Describe the morphology of the red blood cells.
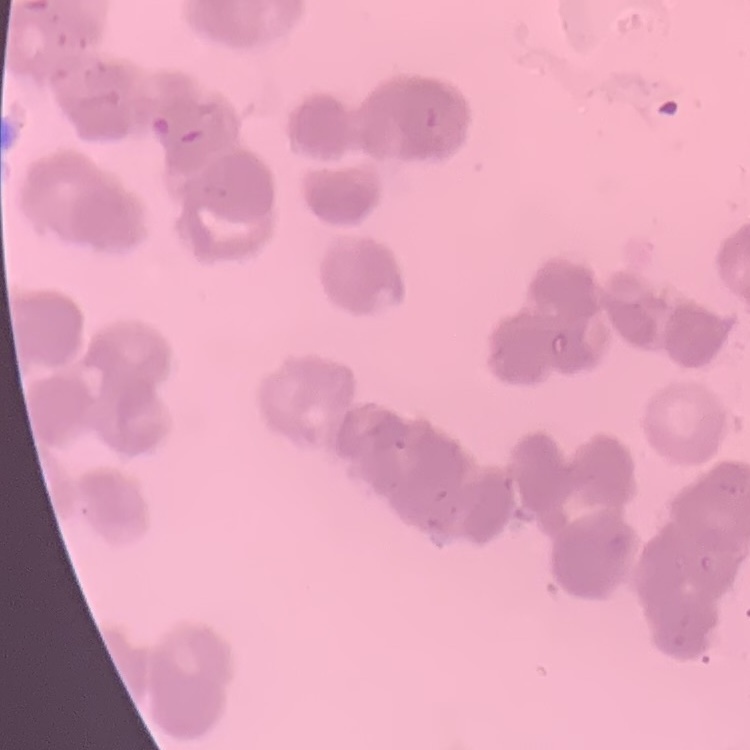
Rouleaux formation.

Summary:
  - Preparation: thin blood smear
  - Stain: Field's or Giemsa
  - Image type: one tile cut from a larger photomicrograph